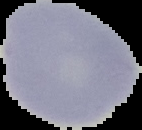

preparation: thin blood film
image_size: 142×130 pixels
result: no malaria parasites seen
image_type: cell region segmented out of the field of view; surrounding area masked to black